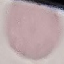
Malaria status: uninfected. Giemsa stain. Automatically extracted cell patch, resized to 64 × 64 pixels. Acquired by smartphone through the microscope eyepiece. Thin blood film.